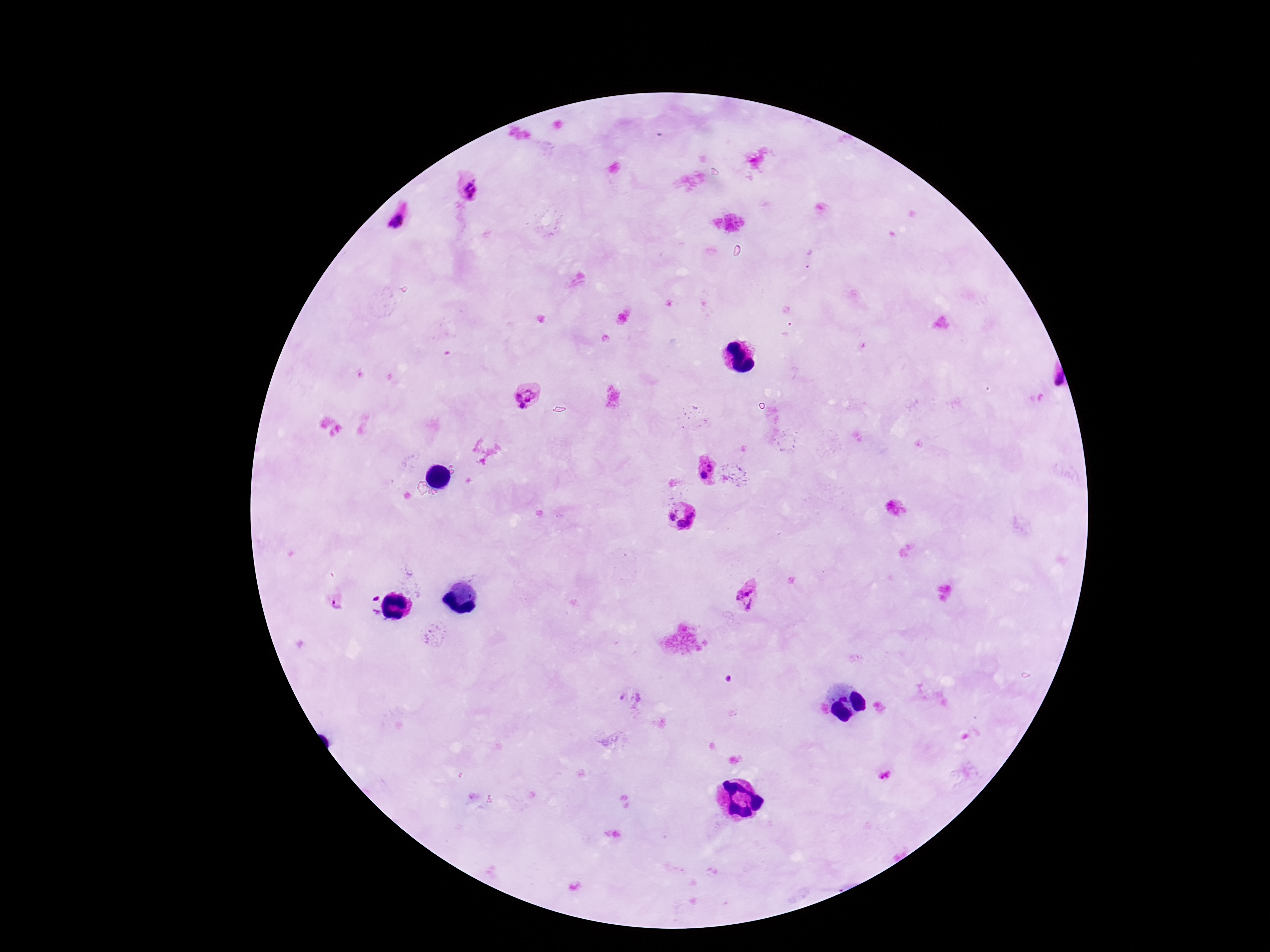

Approximate object centers, in pixels from the top-left corner. Plasmodium parasite locations: (x=471, y=190), (x=395, y=220), (x=1051, y=383), (x=524, y=396), (x=705, y=468), (x=671, y=517), (x=689, y=524), (x=745, y=595), (x=338, y=604), (x=884, y=775). Patient malaria status: positive. Giemsa-stained preparation. 100x magnification. Single field of view. Thick blood smear. Smartphone photograph taken through the microscope eyepiece. Image is 1270×952 pixels.